Identify the parasite.
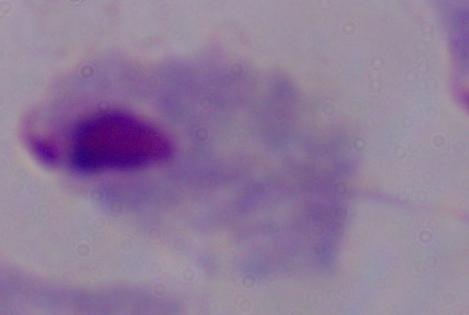
A trichomonad.

Summary:
  - Modality: micrograph
  - Magnification: 1000x